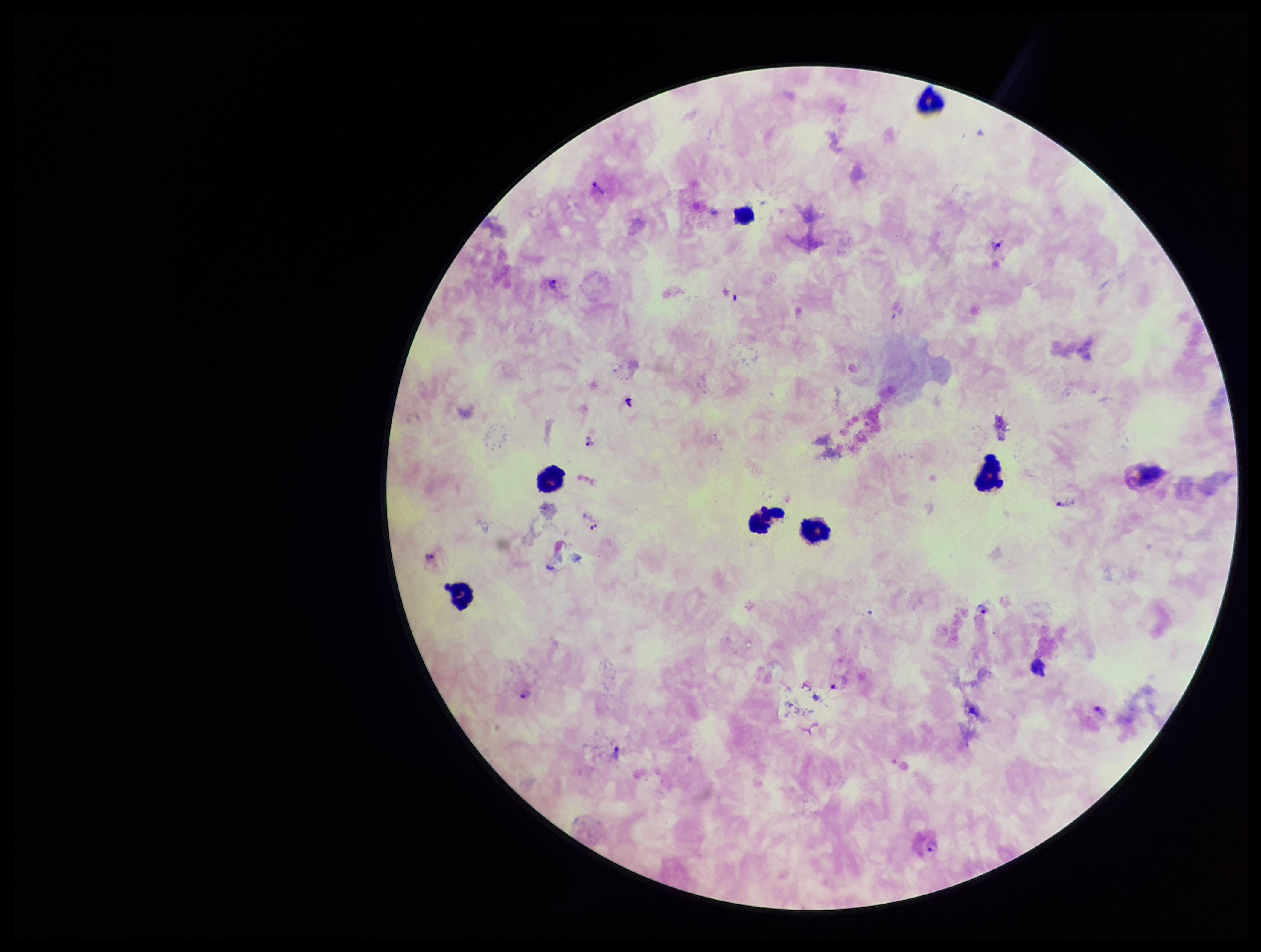
Plasmodium parasites = identified
species reported for this patient = Plasmodium vivax
field of view = single
preparation = thick blood smear
leukocyte count = 8
capture = smartphone photograph through the microscope eyepiece
patient malaria status = positive
image size = 1261×952 pixels
parasite count = 13
stain = Giemsa